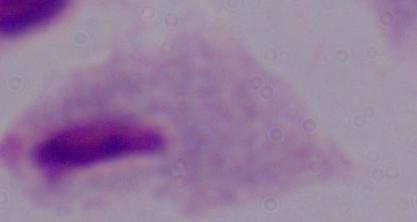
Summary:
  - Magnification: 1000x
  - Modality: micrograph
  - Identification: trichomonad